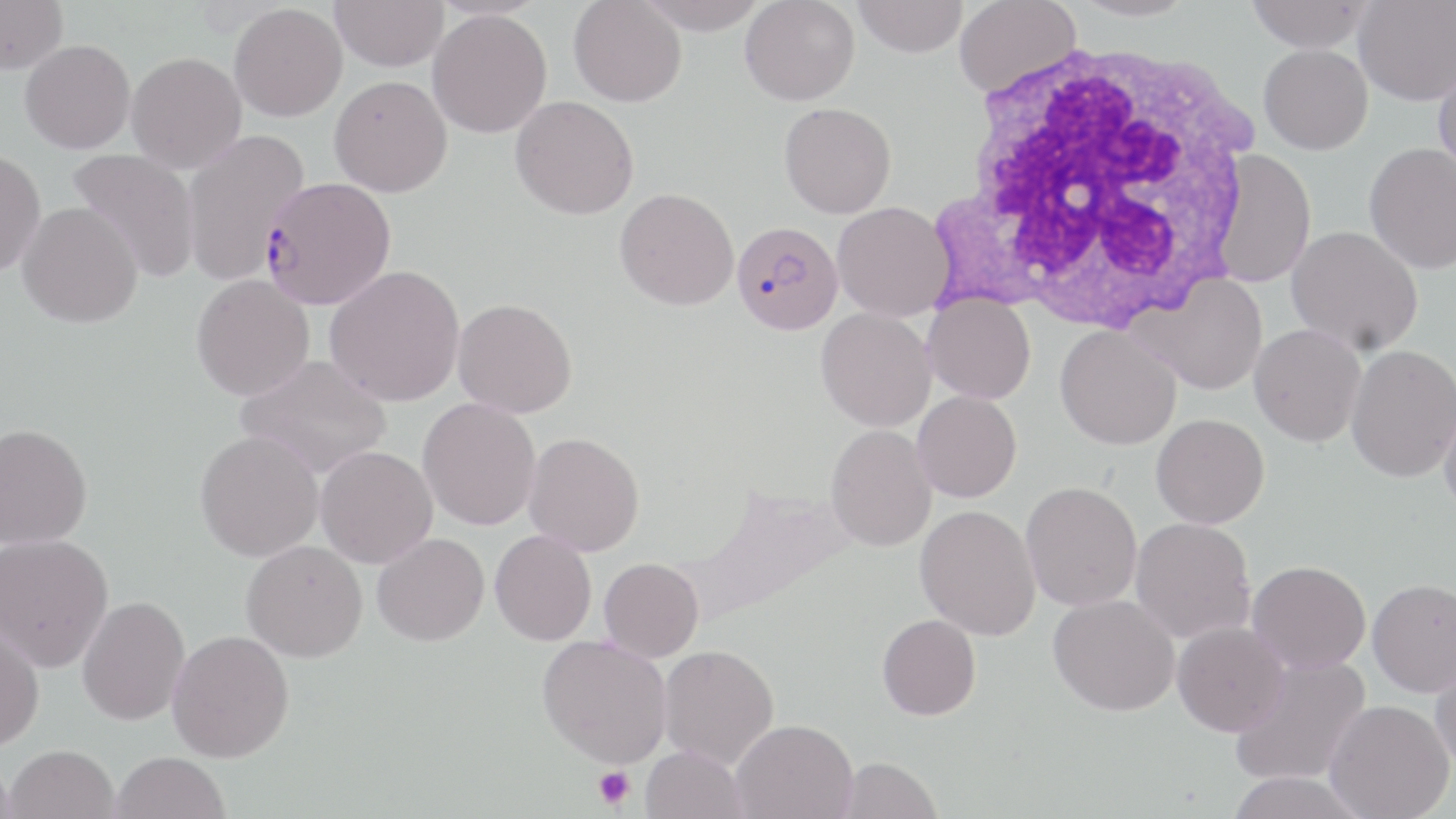
slide_level_diagnosis: Plasmodium falciparum
modality: light microscopy
uninfected_red_blood_cell_locations: 'approximate bounding boxes as (x1, y1, x2, y2) in pixels: (0, 0, 68, 74), (330, 0, 448, 71), (636, 0, 770, 34), (740, 0, 860, 106), (853, 0, 967, 57), (953, 0, 1083, 98), (1066, 0, 1198, 21), (1246, 0, 1373, 52), (1353, 0, 1455, 106), (568, 1, 687, 107), (229, 3, 347, 122), (427, 9, 552, 138), (20, 40, 135, 154), (1259, 44, 1373, 154), (127, 51, 246, 173), (1433, 62, 1456, 182), (329, 75, 452, 197), (510, 96, 639, 220), (779, 102, 896, 218), (181, 127, 310, 286), (1364, 142, 1456, 274), (0, 148, 46, 277), (68, 148, 200, 283), (1212, 151, 1316, 288), (615, 188, 739, 310), (18, 201, 144, 328), (832, 201, 953, 320), (1286, 225, 1423, 356), (324, 265, 465, 407), (1132, 274, 1267, 395), (190, 275, 315, 401), (923, 294, 1036, 404), (453, 298, 577, 418), (815, 308, 936, 431), (1249, 324, 1366, 446), (1055, 325, 1181, 450), (1345, 344, 1455, 482), (236, 354, 393, 480), (912, 391, 1021, 503), (417, 397, 541, 531), (1438, 399, 1456, 517), (1151, 414, 1269, 529), (0, 423, 93, 549), (825, 425, 936, 551), (194, 430, 324, 561), (523, 432, 645, 556), (314, 445, 438, 568), (1020, 481, 1142, 611), (915, 505, 1041, 641), (1130, 517, 1256, 644), (490, 529, 597, 645), (0, 533, 114, 672), (372, 533, 489, 646), (240, 540, 367, 662), (599, 557, 704, 662), (1247, 560, 1370, 673), (1367, 577, 1456, 697), (1048, 594, 1179, 716), (77, 595, 190, 726), (877, 614, 981, 720), (0, 617, 45, 752), (1172, 621, 1290, 736), (167, 629, 295, 763), (537, 635, 672, 769), (659, 644, 779, 769), (1430, 654, 1456, 773), (1229, 655, 1371, 788), (1324, 700, 1454, 819), (732, 719, 858, 818), (5, 744, 120, 819), (640, 746, 748, 819), (111, 751, 231, 819), (835, 756, 943, 819), (0, 758, 17, 818), (1225, 771, 1370, 819)'
plasmodium_falciparum_infected_red_blood_cell_locations: 'approximate bounding boxes as (x1, y1, x2, y2) in pixels: (257, 178, 401, 306), (731, 221, 843, 335)'
stain: May-Grünwald-Giemsa
magnification: 1000x
white_blood_cell_locations: 'approximate bounding boxes as (x1, y1, x2, y2) in pixels: (942, 35, 1269, 334)'
field_of_view: single
image_size: 1456×819 pixels
preparation: thin blood film
platelet_locations: 'approximate bounding boxes as (x1, y1, x2, y2) in pixels: (594, 765, 635, 810)'